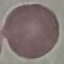
Malaria status: uninfected. Acquired by smartphone through the microscope eyepiece. Giemsa-stained preparation. Thin smear of blood. Cell patch, automatically extracted from a larger field of view and resized to 64 × 64 pixels.